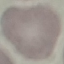
Summary:
  - Result: no malaria parasites detected
  - Preparation: thin blood film
  - Capture: smartphone camera at the microscope eyepiece
  - Image type: automatically extracted cell patch, resized to 64 × 64 pixels
  - Stain: Giemsa